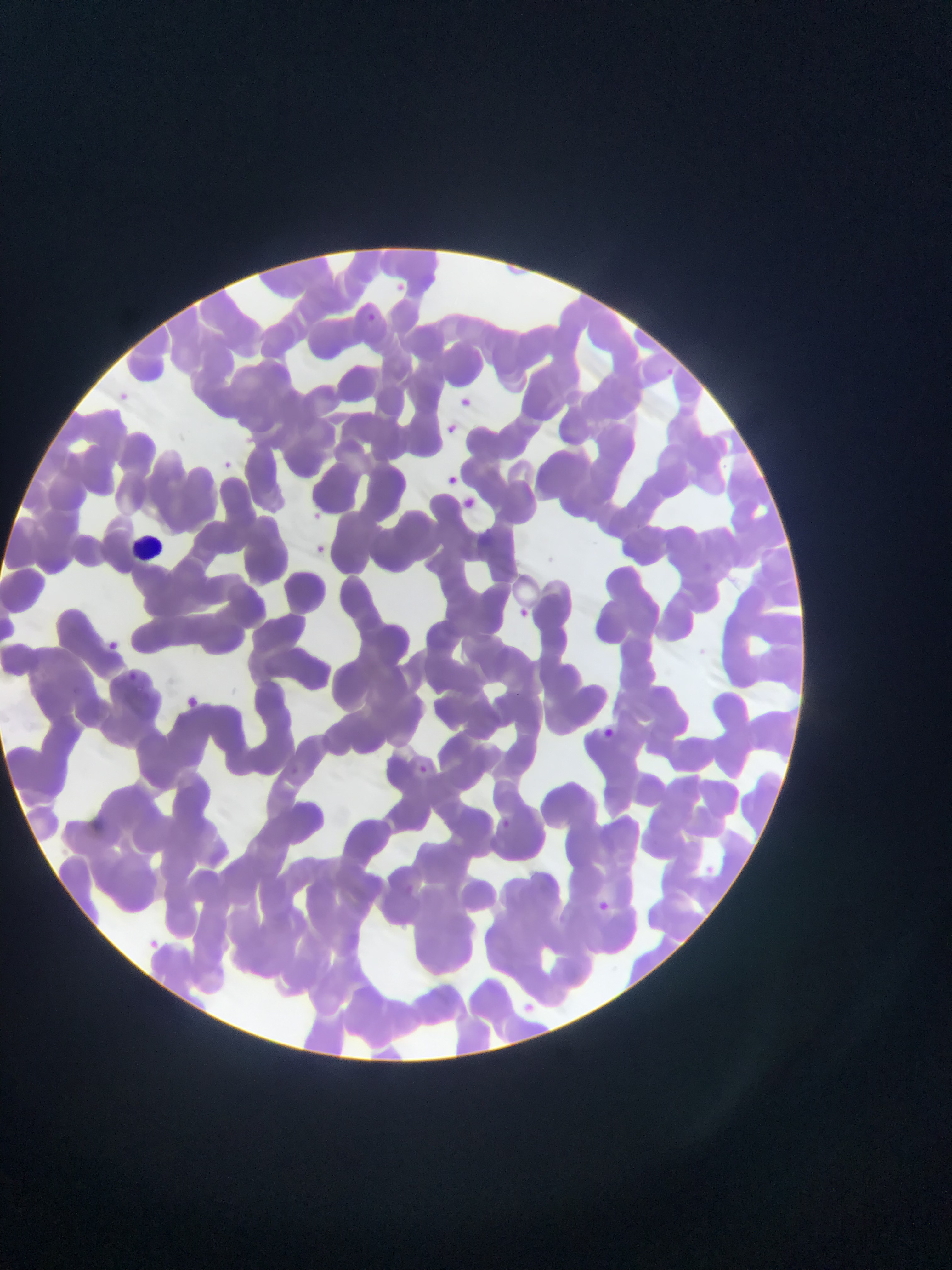

Approximate bounding boxes as {left, top, right, bottom} in pixels.
Summary:
  - Malaria parasite locations: {390, 277, 411, 297}, {358, 308, 383, 330}, {662, 364, 677, 379}, {107, 386, 136, 411}, {454, 392, 478, 413}, {439, 421, 460, 438}, {214, 457, 238, 478}, {443, 472, 459, 489}, {440, 478, 466, 501}, {459, 494, 479, 513}, {306, 506, 327, 526}, {310, 541, 334, 563}, {511, 605, 533, 625}, {102, 636, 124, 655}, {183, 694, 201, 710}, {599, 725, 619, 744}, {413, 760, 432, 779}, {593, 899, 612, 917}, {143, 934, 165, 954}, {518, 991, 540, 1013}
  - Leukocyte locations: {121, 522, 184, 573}
  - Capture: mobile-phone photograph through a microscope
  - Country: Ghana
  - Image size: 952×1270 pixels
  - Field of view: single
  - Preparation: thin blood film